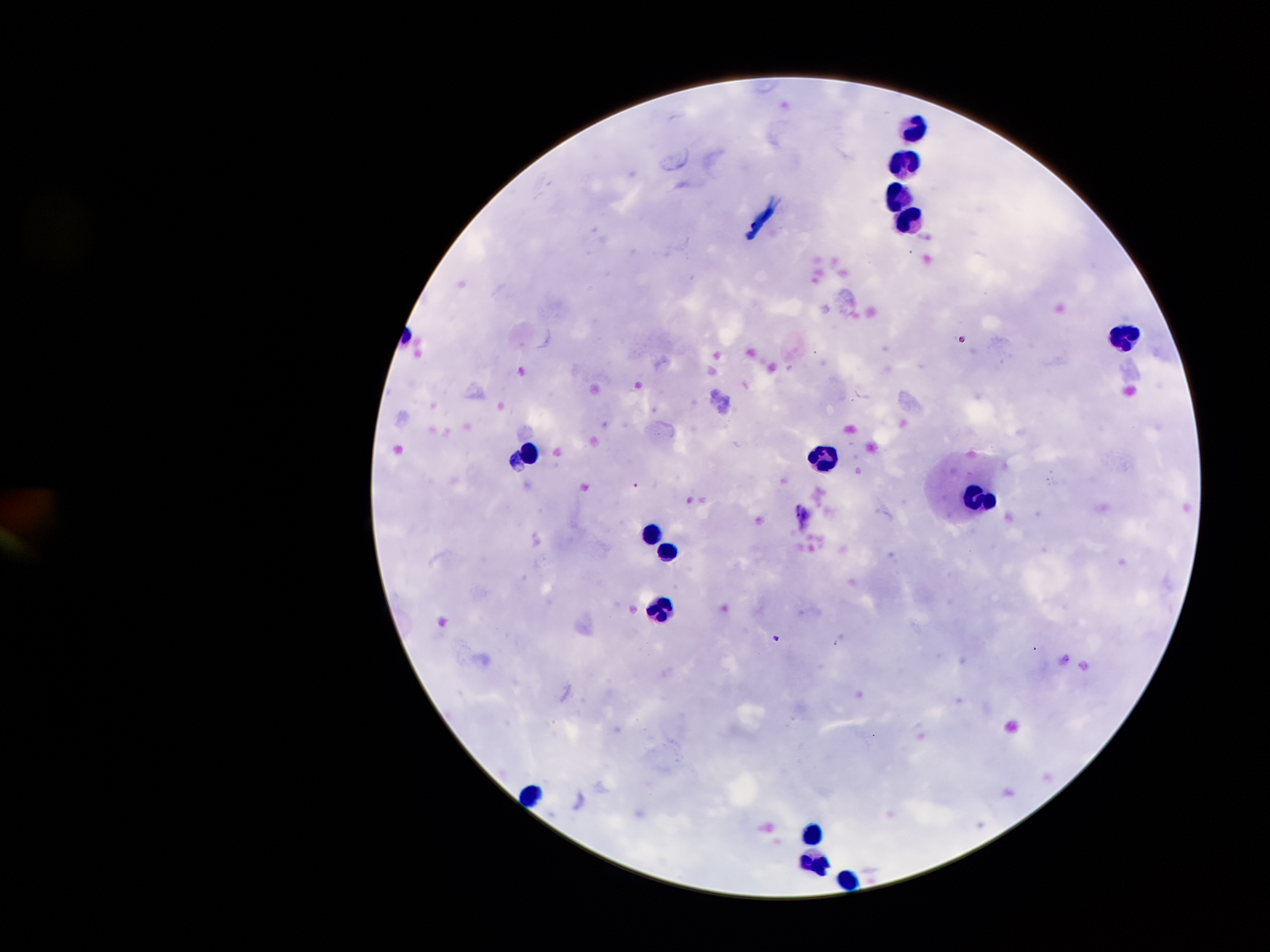
Approximate object centers, in pixels from the top-left corner.
Summary:
  - Leukocyte locations: (x=916, y=127), (x=905, y=161), (x=895, y=192), (x=906, y=216), (x=1123, y=335), (x=531, y=449), (x=825, y=456), (x=982, y=494), (x=651, y=530), (x=671, y=550), (x=660, y=607), (x=527, y=791), (x=809, y=827), (x=811, y=859), (x=846, y=876)
  - Plasmodium parasite locations: (x=963, y=340), (x=636, y=486), (x=778, y=638)
  - Stain: Giemsa
  - Patient malaria status: infected with Plasmodium falciparum
  - Capture: smartphone through the microscope eyepiece
  - Preparation: thick peripheral-blood smear
  - Image size: 1270×952 pixels
  - Field of view: single
  - Magnification: 100x